Locate every blood parasite and identify its species.
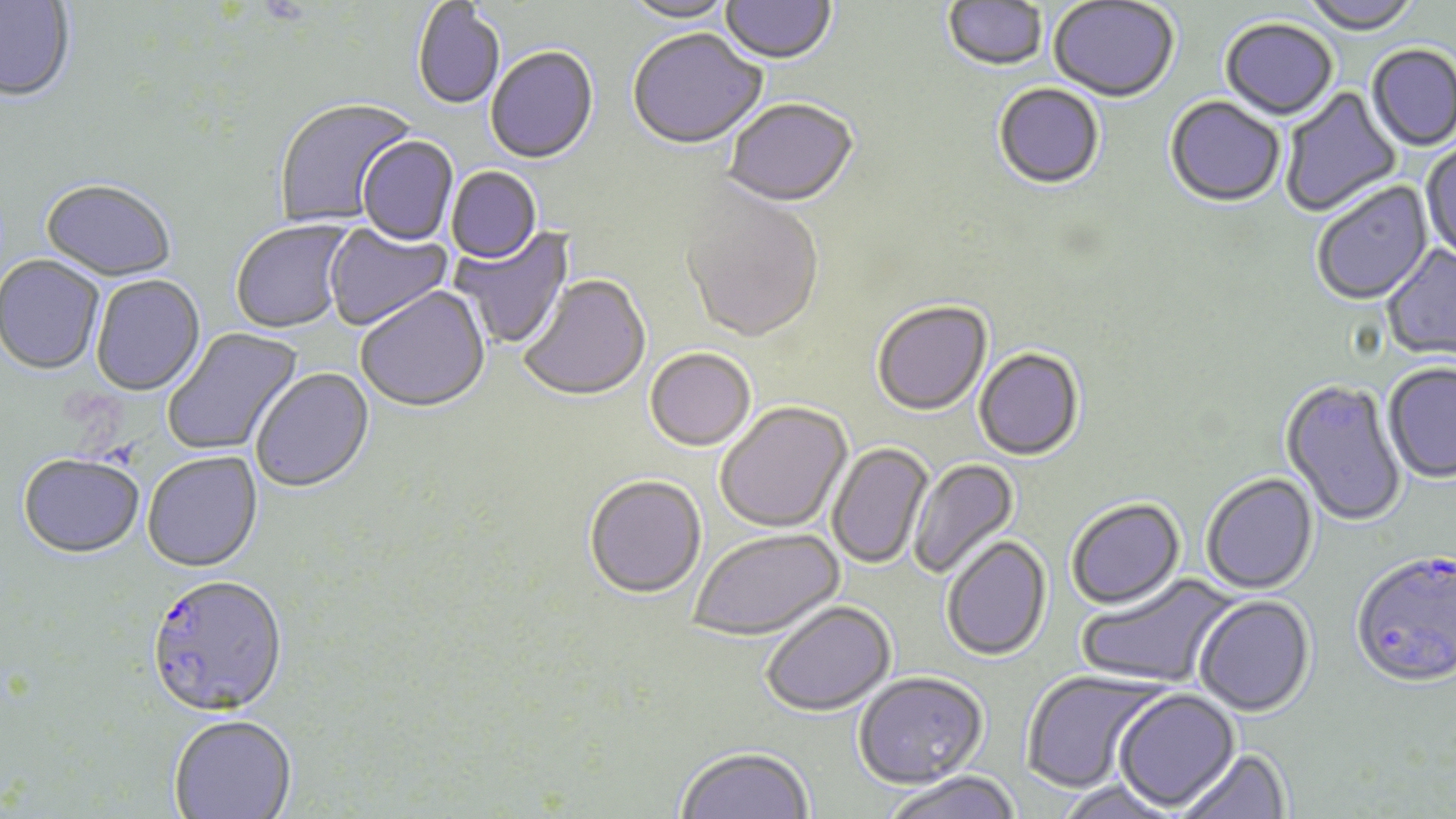
Approximate bounding boxes as (x1,y1)-(x2,y2) corner pairs in pixels.
Plasmodium falciparum-infected red blood cells: (1351,555)-(1456,691), (145,575)-(288,720).
No Plasmodium ovale, Plasmodium malariae, Plasmodium vivax, Babesia divergens, or Trypanosoma brucei observed.

Uninfected red blood cell locations: (0,0)-(76,104), (621,0)-(738,25), (721,0)-(836,66), (1048,0)-(1179,104), (1301,0)-(1421,36), (943,1)-(1048,73), (412,2)-(505,111), (1220,20)-(1338,122), (627,31)-(767,152), (1367,46)-(1456,152), (486,48)-(599,166), (994,84)-(1105,191), (1280,86)-(1403,217), (274,98)-(419,229), (1165,98)-(1285,209), (723,100)-(860,210), (357,137)-(458,247), (1421,141)-(1456,264), (447,167)-(542,265), (39,182)-(177,285), (1312,182)-(1435,308), (679,186)-(825,346), (229,219)-(356,336), (324,224)-(454,333), (450,227)-(576,351), (1381,244)-(1456,363), (0,256)-(104,376), (518,275)-(652,404), (90,276)-(206,397), (356,287)-(491,415), (872,302)-(993,418), (163,327)-(304,456), (645,349)-(756,453), (974,349)-(1084,462), (1383,364)-(1456,485), (251,369)-(375,494), (1280,380)-(1407,529), (715,403)-(853,534), (828,442)-(933,570), (143,452)-(263,573), (17,455)-(145,560), (908,458)-(1020,580), (1201,473)-(1319,595), (584,477)-(706,601), (1066,499)-(1186,611), (689,529)-(845,643), (942,537)-(1052,662), (1075,573)-(1238,690), (1194,596)-(1315,718), (761,601)-(897,718), (1021,670)-(1169,795), (854,673)-(988,791), (1113,690)-(1241,812), (169,715)-(297,819), (675,746)-(813,819), (1176,748)-(1291,819), (882,772)-(1022,819), (1054,780)-(1183,819). Slide-level diagnosis: Plasmodium falciparum. Optical microscopy. May-Grünwald-Giemsa stain. Single field of view. Image is 1456×819 pixels. Thin blood smear. Captured at 1000x magnification.